Comment on the morphology of the erythrocytes.
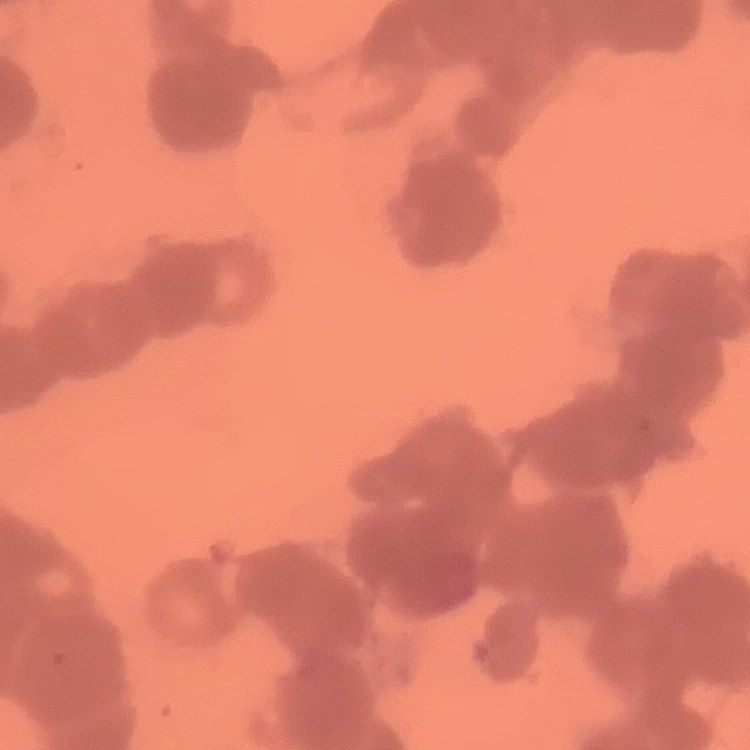

Rouleaux formation.

Summary:
  - Preparation: thin blood film
  - Image type: square crop of a larger photomicrograph
  - Stain: Field's or Giemsa